Name the parasite shown.
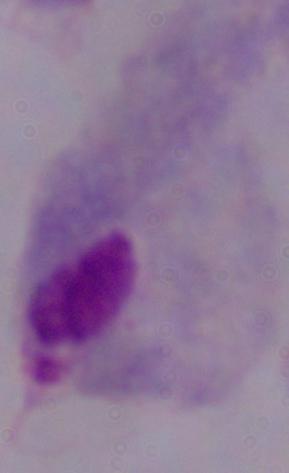

A trichomonad.

modality = photomicrograph
magnification = 1000x